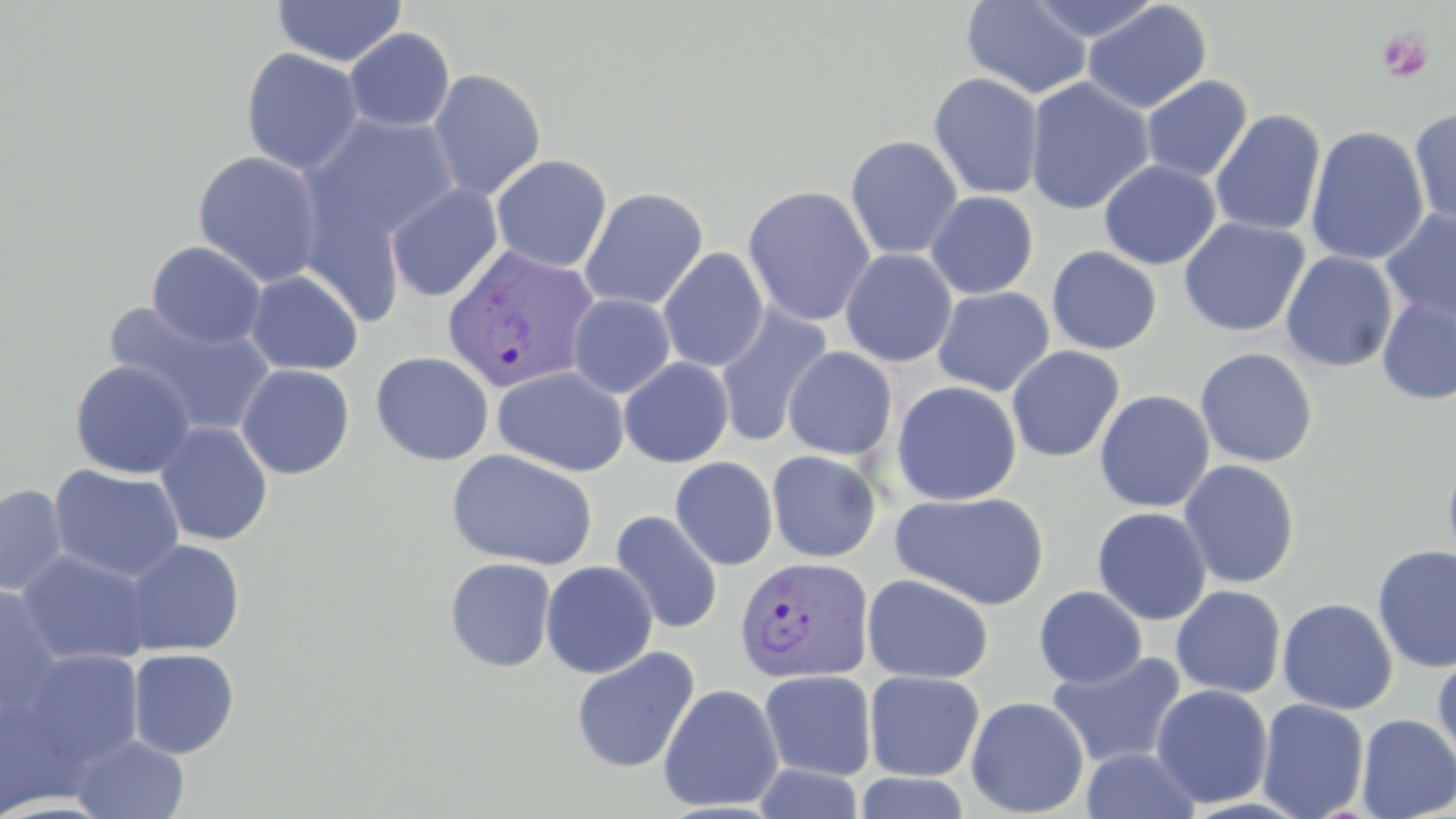 Approximate bounding boxes as (x1,y1)-(x2,y2) corner pairs in pixels. Plasmodium vivax-infected red blood cell locations: (442,244)-(600,393), (735,555)-(875,684). Platelet locations: (1376,27)-(1434,83). Uninfected red blood cell locations: (961,0)-(1093,99), (1025,0)-(1164,43), (272,1)-(408,67), (1082,1)-(1212,114), (343,27)-(455,133), (240,47)-(365,175), (426,68)-(546,201), (928,73)-(1044,200), (1141,75)-(1253,183), (1024,77)-(1155,215), (1408,106)-(1456,230), (1210,110)-(1327,236), (301,112)-(463,257), (1305,125)-(1429,266), (845,135)-(963,260), (192,150)-(325,287), (491,154)-(611,272), (1098,159)-(1221,270), (385,183)-(503,302), (742,185)-(877,326), (579,187)-(708,311), (924,191)-(1039,299), (1380,208)-(1456,330), (1178,217)-(1310,337), (146,241)-(267,349), (1047,246)-(1162,355), (658,248)-(769,372), (840,248)-(957,367), (1280,251)-(1398,372), (245,270)-(363,375), (932,286)-(1055,396), (568,293)-(676,398), (1376,297)-(1456,405), (105,301)-(277,438), (714,303)-(833,447), (783,346)-(898,461), (1005,346)-(1125,463), (1195,348)-(1318,468), (370,351)-(495,466), (618,357)-(735,468), (69,360)-(196,479), (236,364)-(355,480), (492,366)-(630,476), (891,380)-(1022,506), (1094,389)-(1215,513), (154,421)-(274,546), (446,448)-(598,571), (766,449)-(882,562), (1442,450)-(1456,579), (670,456)-(779,571), (1178,460)-(1300,588), (48,464)-(186,583), (0,484)-(70,596), (891,490)-(1049,610), (1092,506)-(1212,625), (610,510)-(725,635), (121,539)-(246,657), (1372,545)-(1456,673), (16,549)-(156,667), (444,557)-(557,672), (540,560)-(658,679), (862,572)-(994,684), (0,585)-(67,718), (1171,585)-(1286,699), (1034,586)-(1147,689), (1277,597)-(1398,715), (571,646)-(700,774), (128,647)-(240,759), (17,649)-(145,771), (1046,650)-(1187,769), (1432,651)-(1456,769), (759,670)-(877,781), (863,670)-(985,781), (658,683)-(784,812), (1151,683)-(1273,808), (0,695)-(88,818), (965,696)-(1089,817), (1256,697)-(1370,819), (1355,713)-(1456,818), (69,733)-(190,818), (1079,746)-(1203,819), (753,763)-(867,819), (853,772)-(972,818). Slide-level diagnosis: Plasmodium vivax. One field of a larger specimen. 1000x magnification. Thin blood film. Image is 1456×819 pixels. May-Grünwald-Giemsa-stained preparation. Light microscopy.